Assess the morphology of the erythrocytes.
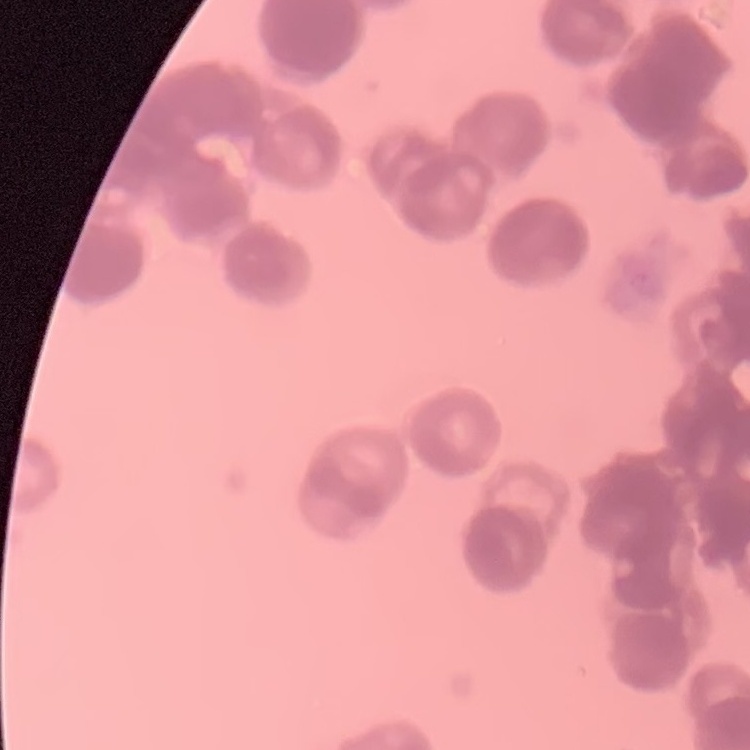

Rouleaux formation.

preparation = thin peripheral smear
stain = Field's or Giemsa
image type = one tile cut from a larger photomicrograph